State the blood parasite species.
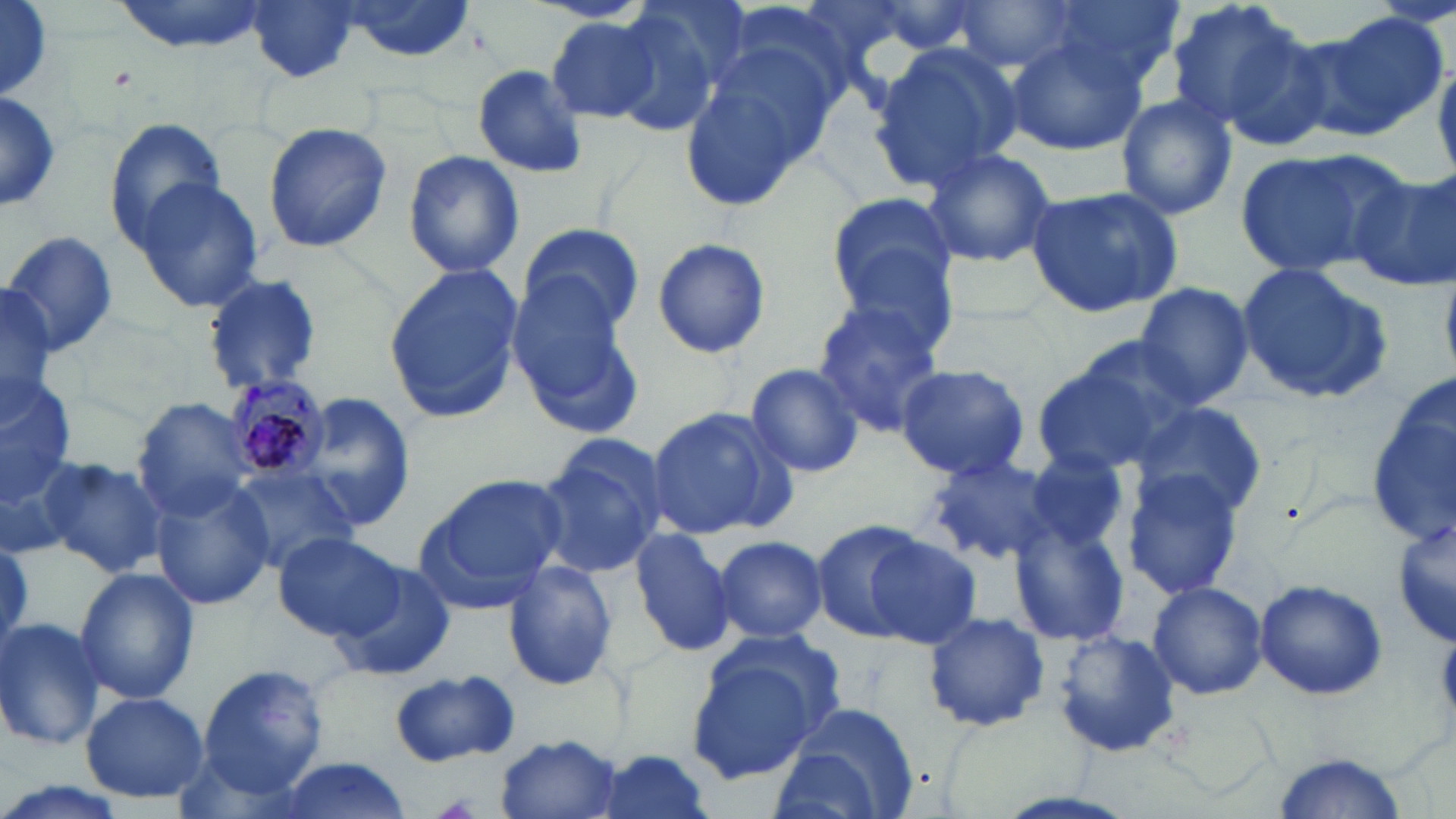

Plasmodium malariae.

Summary:
  - Coordinate format: approximate bounding boxes as (x1, y1, x2, y2) in pixels
  - Platelet locations: (1436, 637, 1456, 713), (434, 793, 483, 819)
  - Uninfected red blood cell locations: (110, 0, 271, 55), (244, 0, 361, 84), (342, 0, 479, 62), (1166, 0, 1314, 137), (608, 1, 741, 138), (1045, 1, 1183, 95), (946, 2, 1082, 73), (0, 5, 56, 100), (1304, 14, 1446, 139), (544, 15, 663, 124), (1220, 26, 1346, 155), (999, 32, 1146, 159), (867, 40, 1021, 191), (681, 41, 839, 208), (474, 65, 591, 178), (0, 88, 62, 214), (0, 91, 63, 211), (1115, 94, 1237, 220), (105, 115, 228, 250), (262, 123, 393, 252), (919, 145, 1058, 269), (1231, 148, 1400, 277), (403, 151, 525, 278), (1352, 169, 1456, 292), (130, 175, 265, 313), (1024, 186, 1184, 319), (826, 192, 958, 313), (516, 222, 646, 336), (4, 229, 121, 359), (651, 238, 771, 358), (828, 256, 958, 369), (383, 262, 523, 424), (1237, 263, 1393, 402), (202, 273, 323, 394), (0, 283, 57, 418), (1132, 283, 1254, 409), (512, 285, 648, 434), (811, 300, 946, 432), (1072, 335, 1207, 442), (1031, 355, 1183, 478), (743, 362, 865, 479), (893, 363, 1029, 481), (1368, 366, 1456, 551), (0, 372, 77, 508), (1366, 377, 1456, 545), (295, 391, 413, 529), (132, 399, 257, 518), (1130, 401, 1269, 521), (645, 407, 787, 539), (535, 436, 667, 578), (1023, 449, 1131, 554), (33, 455, 168, 579), (924, 455, 1061, 565), (226, 465, 363, 572), (1119, 466, 1248, 601), (415, 476, 565, 610), (149, 477, 277, 609), (1390, 511, 1453, 650), (809, 519, 923, 640), (1008, 520, 1131, 645), (627, 527, 735, 656), (273, 531, 404, 642), (715, 534, 827, 641), (0, 535, 32, 658), (864, 535, 981, 649), (503, 562, 620, 689), (331, 564, 457, 681), (75, 566, 199, 705), (1253, 577, 1387, 701), (1147, 580, 1269, 700), (922, 611, 1050, 731), (0, 616, 106, 751), (1053, 629, 1182, 758), (686, 632, 842, 786), (195, 662, 330, 796), (389, 670, 521, 766), (81, 690, 210, 806), (775, 702, 920, 819), (494, 733, 623, 818), (588, 749, 718, 819), (1268, 753, 1408, 818), (272, 757, 414, 819), (0, 781, 126, 819)
  - Plasmodium malariae-infected red blood cell locations: (224, 375, 330, 484)
  - Magnification: 1000x
  - Field of view: single
  - Stain: May-Grünwald-Giemsa
  - Modality: optical microscopy
  - Image size: 1456×819 pixels
  - Preparation: thin blood film